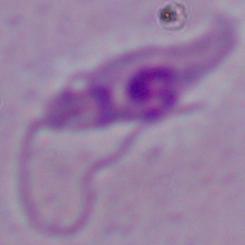
modality = photomicrograph
identification = Leishmania
magnification = 1000x